Locate every blood parasite and identify its species.
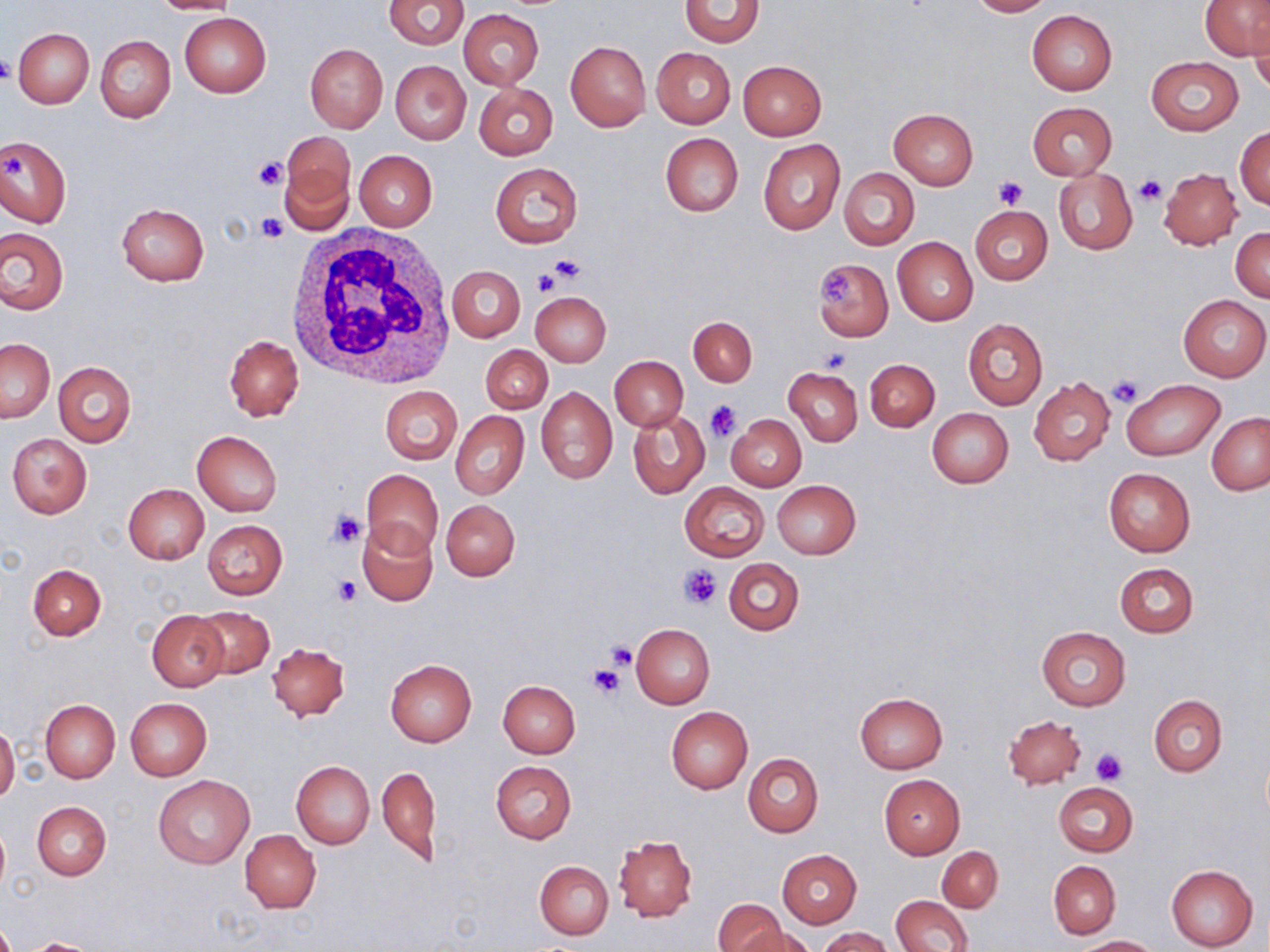
No blood parasites observed.

{
  "slide_level_diagnosis": "negative for blood parasites",
  "image_size": "1270×952 pixels",
  "uninfected_red_blood_cell_locations": "approximate bounding boxes as [x1, y1, x2, y2] in pixels: [149, 0, 240, 16], [383, 0, 468, 49], [679, 0, 764, 47], [967, 0, 1053, 17], [1202, 1, 1268, 61], [458, 9, 544, 89], [1026, 10, 1118, 95], [179, 13, 270, 97], [1249, 17, 1270, 96], [13, 28, 93, 108], [96, 34, 175, 123], [566, 41, 651, 131], [304, 44, 388, 132], [651, 47, 736, 128], [1145, 57, 1242, 135], [390, 60, 471, 144], [738, 60, 826, 139], [473, 82, 558, 160], [1027, 102, 1117, 180], [888, 109, 977, 189], [1236, 126, 1270, 209], [283, 132, 355, 206], [660, 133, 743, 217], [0, 134, 72, 228], [759, 140, 844, 235], [354, 150, 438, 230], [278, 161, 354, 237], [491, 163, 581, 248], [839, 168, 919, 249], [1158, 168, 1242, 249], [1053, 169, 1138, 255], [116, 203, 210, 286], [970, 206, 1053, 285], [0, 227, 67, 315], [1231, 227, 1270, 302], [892, 237, 977, 325], [813, 260, 893, 340], [446, 265, 525, 343], [530, 291, 611, 367], [1178, 295, 1269, 381], [689, 316, 757, 386], [963, 317, 1047, 409], [224, 336, 303, 422], [1, 339, 54, 422], [481, 345, 551, 414], [610, 356, 687, 431], [865, 358, 939, 432], [53, 362, 136, 447], [783, 368, 862, 446], [1029, 377, 1116, 466], [1122, 379, 1223, 460], [380, 385, 462, 464], [536, 386, 618, 484], [627, 408, 709, 499], [926, 408, 1014, 487], [450, 411, 529, 499], [1207, 412, 1270, 496], [726, 414, 806, 491], [192, 431, 283, 516], [6, 433, 92, 517], [1103, 467, 1195, 557], [361, 468, 442, 558], [772, 480, 860, 559], [681, 483, 769, 561], [122, 484, 209, 565], [441, 499, 520, 581], [202, 519, 286, 600], [358, 521, 438, 606], [724, 558, 804, 635], [1114, 562, 1198, 637], [28, 564, 106, 640], [192, 606, 275, 679], [148, 612, 227, 691], [631, 623, 714, 709], [1036, 627, 1130, 711], [266, 641, 348, 722], [385, 659, 477, 746], [498, 680, 580, 757], [855, 692, 947, 772], [1148, 695, 1227, 776], [125, 697, 213, 780], [40, 699, 121, 782], [666, 706, 753, 793], [1004, 715, 1086, 789], [0, 722, 19, 804], [743, 753, 823, 835], [291, 760, 375, 850], [491, 761, 577, 843], [378, 764, 441, 866], [153, 775, 254, 868], [878, 775, 965, 858], [1053, 782, 1138, 856], [32, 801, 111, 881], [0, 821, 9, 896], [241, 830, 321, 913], [613, 835, 697, 921], [937, 846, 1003, 912], [777, 849, 862, 927], [535, 861, 614, 939], [1049, 861, 1120, 938], [1166, 864, 1257, 951], [892, 895, 972, 952], [713, 899, 788, 952], [736, 927, 815, 952], [818, 927, 896, 952], [1074, 935, 1159, 951], [20, 938, 104, 952]",
  "stain": "May-Grünwald-Giemsa",
  "platelet_locations": "approximate bounding boxes as [x1, y1, x2, y2] in pixels: [0, 54, 14, 84], [252, 156, 289, 190], [995, 176, 1027, 208], [1135, 176, 1165, 205], [255, 212, 288, 242], [548, 255, 587, 284], [531, 268, 558, 296], [820, 269, 858, 308], [819, 348, 851, 374], [1107, 375, 1144, 409], [704, 399, 742, 441], [327, 509, 367, 548], [680, 565, 721, 608], [332, 573, 361, 605], [606, 641, 638, 670], [596, 649, 632, 685], [586, 663, 623, 698], [1091, 747, 1128, 786]",
  "magnification": "1000x",
  "field_of_view": "one of a larger specimen",
  "white_blood_cell_locations": "approximate bounding boxes as [x1, y1, x2, y2] in pixels: [284, 223, 454, 388]",
  "preparation": "thin blood smear",
  "modality": "optical microscopy"
}